Outline each blood parasite and name the species.
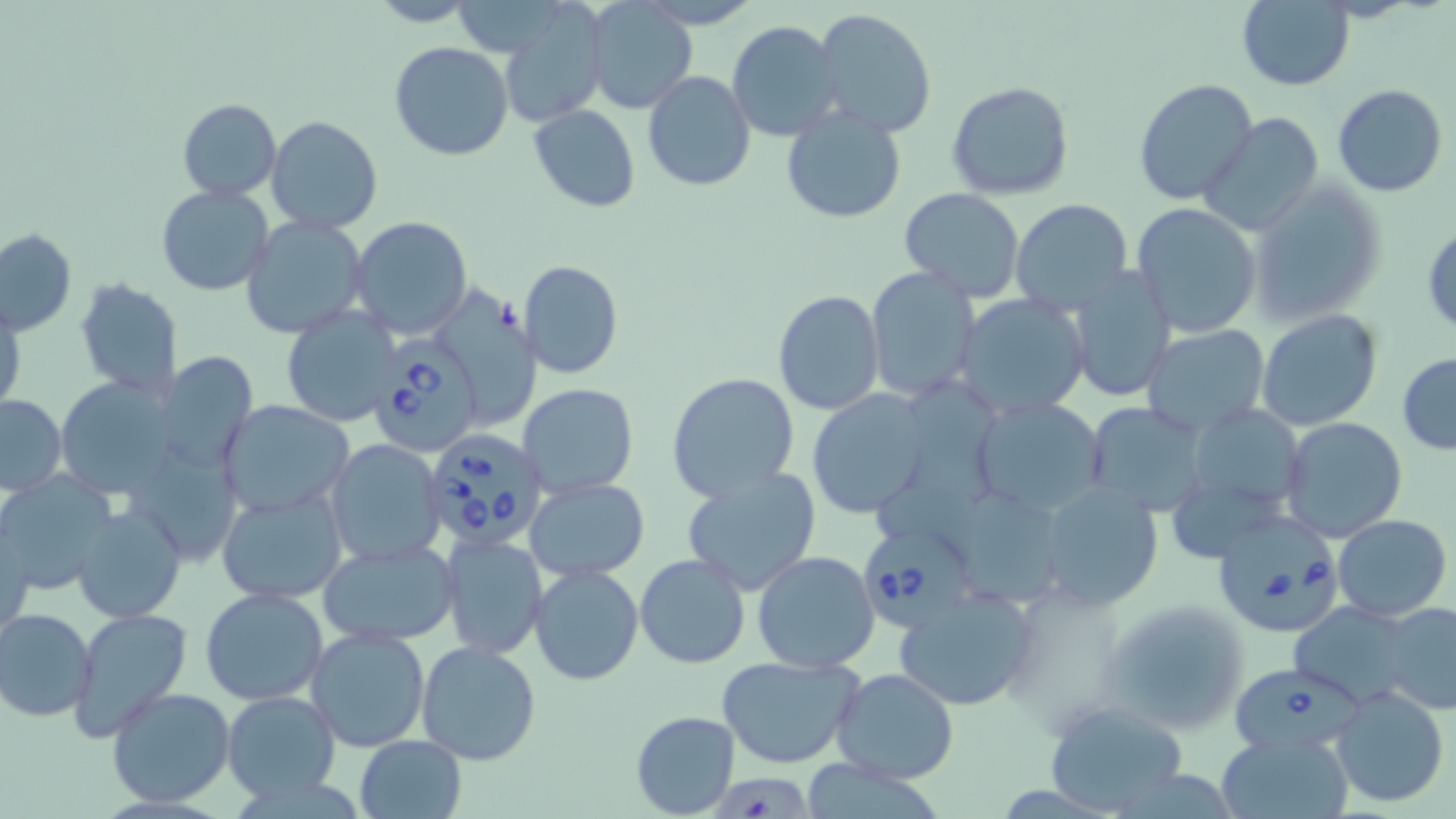
Approximate bounding boxes as [x1, y1, x2, y2] in pixels.
Babesia divergens-infected red blood cells: [372, 342, 483, 456], [420, 426, 552, 552], [1211, 508, 1346, 635], [864, 522, 978, 627], [1228, 662, 1380, 755].
No Plasmodium falciparum, Plasmodium ovale, Plasmodium malariae, Plasmodium vivax, or Trypanosoma brucei observed.

slide-level diagnosis = Babesia divergens
preparation = thin blood film
stain = May-Grünwald-Giemsa
magnification = 1000x
modality = optical microscopy
field of view = single
uninfected red blood cell locations = approximate bounding boxes as [x1, y1, x2, y2] in pixels: [645, 0, 755, 26], [366, 1, 480, 27], [586, 1, 695, 114], [1235, 1, 1354, 89], [498, 2, 611, 127], [812, 8, 939, 139], [726, 20, 844, 141], [389, 41, 515, 162], [643, 71, 756, 191], [1134, 79, 1259, 207], [947, 81, 1075, 201], [1333, 85, 1448, 197], [176, 99, 282, 199], [529, 104, 641, 212], [781, 107, 906, 224], [1201, 112, 1325, 238], [264, 116, 383, 235], [1249, 180, 1388, 325], [155, 185, 274, 296], [900, 187, 1026, 301], [1011, 199, 1134, 316], [1130, 203, 1262, 338], [241, 215, 370, 339], [349, 216, 473, 338], [1423, 222, 1456, 335], [0, 228, 76, 336], [518, 259, 623, 380], [1066, 264, 1177, 404], [865, 267, 980, 403], [75, 278, 183, 398], [442, 284, 548, 430], [773, 289, 885, 413], [957, 293, 1091, 419], [1, 299, 23, 415], [280, 306, 403, 427], [1256, 309, 1385, 431], [1142, 325, 1271, 436], [157, 353, 258, 474], [1397, 354, 1456, 453], [666, 372, 801, 501], [54, 376, 185, 496], [516, 382, 639, 498], [880, 382, 1009, 529], [805, 388, 933, 520], [1, 394, 64, 495], [971, 396, 1108, 518], [1083, 400, 1208, 517], [217, 402, 354, 515], [1181, 403, 1308, 521], [1279, 416, 1408, 543], [324, 440, 446, 567], [681, 467, 823, 596], [2, 473, 114, 592], [524, 478, 650, 582], [1034, 480, 1165, 610], [215, 488, 348, 604], [957, 496, 1057, 603], [74, 503, 186, 623], [1333, 513, 1452, 621], [1, 520, 34, 644], [441, 534, 549, 658], [316, 538, 462, 646], [752, 549, 880, 673], [634, 553, 750, 669], [529, 562, 644, 685], [893, 585, 1039, 712], [200, 587, 329, 707], [1098, 598, 1252, 738], [1290, 602, 1421, 704], [1378, 602, 1456, 715], [67, 607, 194, 743], [0, 608, 97, 723], [305, 624, 432, 754], [416, 640, 543, 767], [718, 652, 864, 770], [831, 668, 960, 783], [1331, 686, 1450, 807], [105, 688, 237, 807], [221, 689, 340, 802], [1041, 700, 1192, 816], [629, 709, 740, 818], [1217, 731, 1353, 818], [354, 734, 467, 818]
image size = 1456×819 pixels